Point out each Plasmodium parasite.
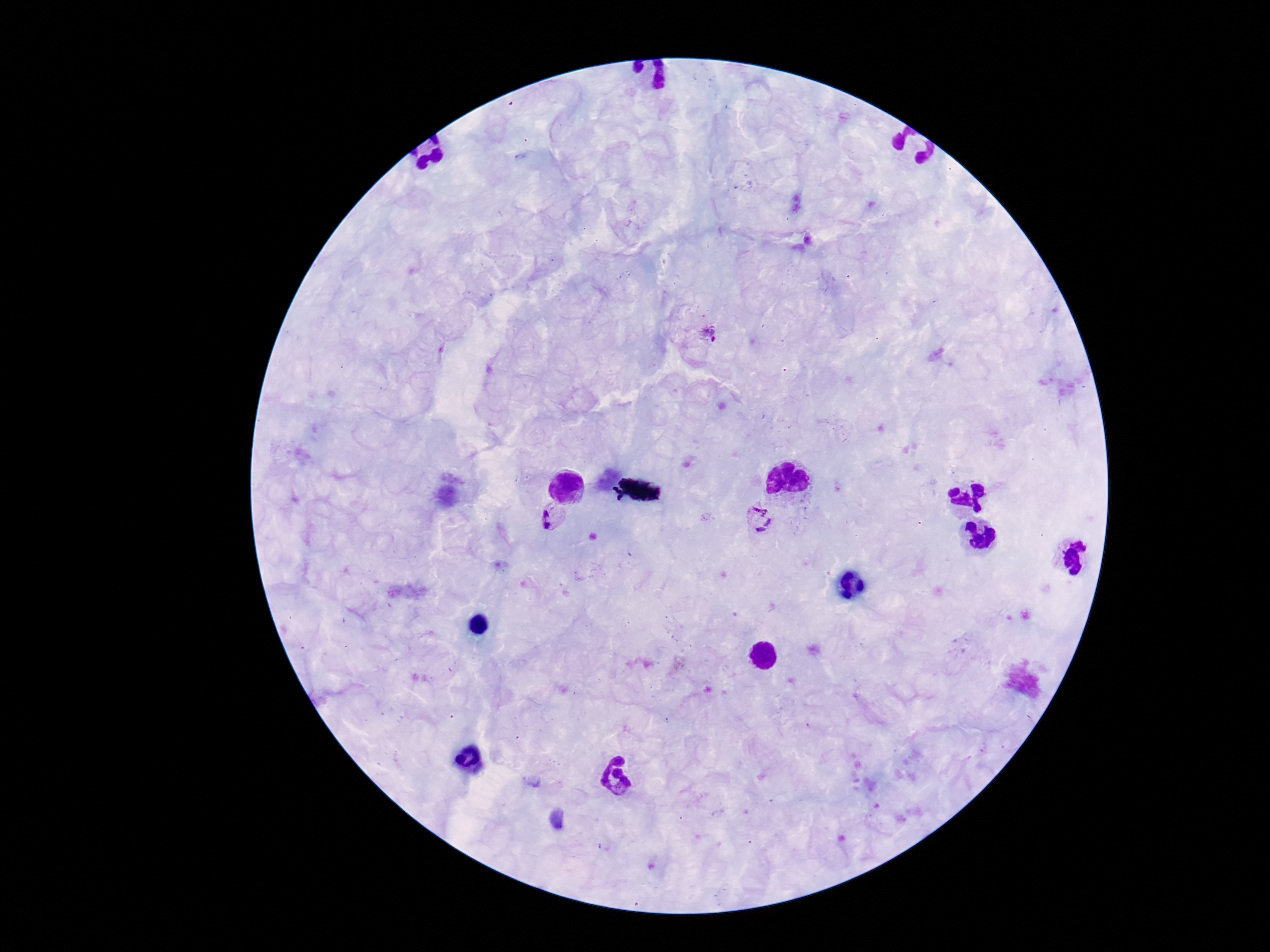

Approximate centers as [x, y] in pixels.
Plasmodium parasites: [704, 332], [552, 518], [757, 518].

capture = smartphone camera through the microscope eyepiece
image size = 1270×952 pixels
magnification = 100x
field of view = single
stain = Giemsa
preparation = thick blood smear
patient malaria status = positive